State the blood parasite species.
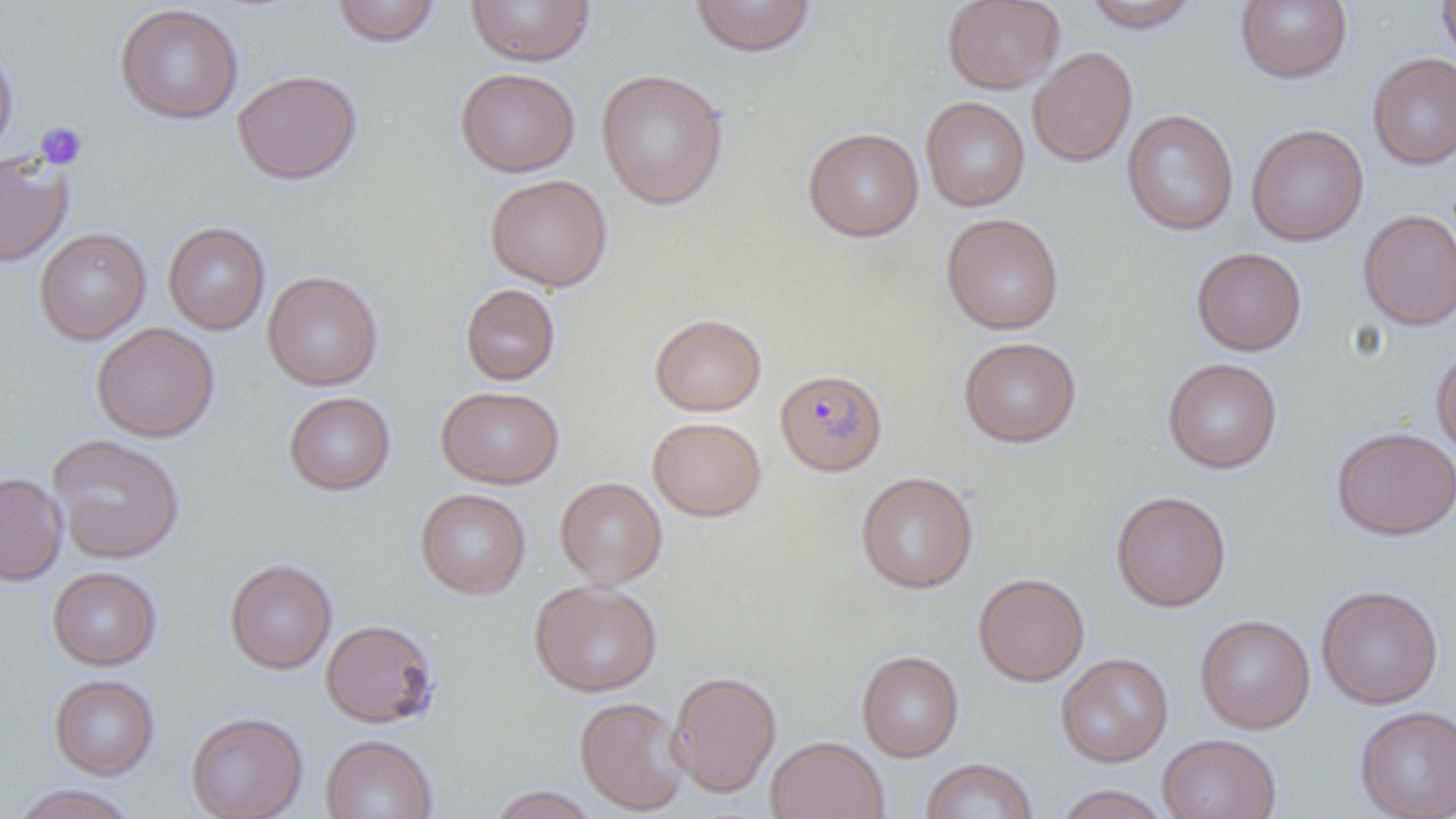

Plasmodium falciparum.

magnification = 1000x
Plasmodium falciparum-infected red blood cell locations = approximate bounding boxes as (x1,y1)-(x2,y2) corner pairs in pixels: (779,376)-(887,475)
field of view = one of a larger specimen
preparation = thin blood smear
uninfected red blood cell locations = approximate bounding boxes as (x1,y1)-(x2,y2) corner pairs in pixels: (465,0)-(595,67), (689,0)-(817,57), (942,0)-(1065,94), (1083,0)-(1202,33), (1235,0)-(1352,84), (1437,0)-(1456,70), (331,1)-(441,47), (114,4)-(243,124), (0,43)-(18,162), (1027,46)-(1138,168), (1367,53)-(1456,170), (455,67)-(580,177), (232,69)-(361,185), (595,69)-(729,210), (921,97)-(1030,212), (1121,109)-(1239,236), (1246,124)-(1369,246), (803,127)-(924,242), (0,153)-(73,267), (485,174)-(612,291), (1358,209)-(1456,330), (941,212)-(1065,335), (162,222)-(270,335), (33,227)-(151,345), (1191,247)-(1307,356), (262,271)-(383,391), (460,284)-(561,385), (649,313)-(767,416), (91,322)-(219,442), (959,337)-(1082,447), (1431,343)-(1456,462), (1162,357)-(1282,474), (436,386)-(564,489), (283,391)-(395,495), (647,417)-(766,521), (1331,426)-(1456,541), (47,433)-(185,565), (855,472)-(978,594), (0,473)-(67,586), (555,477)-(667,587), (415,488)-(530,599), (1110,490)-(1232,613), (224,558)-(337,674), (47,567)-(162,671), (973,572)-(1090,687), (529,580)-(663,697), (1316,585)-(1444,709), (1195,614)-(1315,734), (320,619)-(440,728), (856,650)-(964,762), (1055,652)-(1173,767), (667,670)-(781,798), (49,674)-(159,780), (574,696)-(689,816), (1355,706)-(1456,818), (185,712)-(308,819), (1157,733)-(1281,819), (320,734)-(438,819), (765,736)-(889,819), (920,758)-(1038,819), (9,784)-(142,819), (1053,784)-(1171,819), (487,785)-(600,818)
platelet locations = approximate bounding boxes as (x1,y1)-(x2,y2) corner pairs in pixels: (34,121)-(88,171)
image size = 1456×819 pixels
modality = light microscopy